Describe the morphology of the red blood cells.
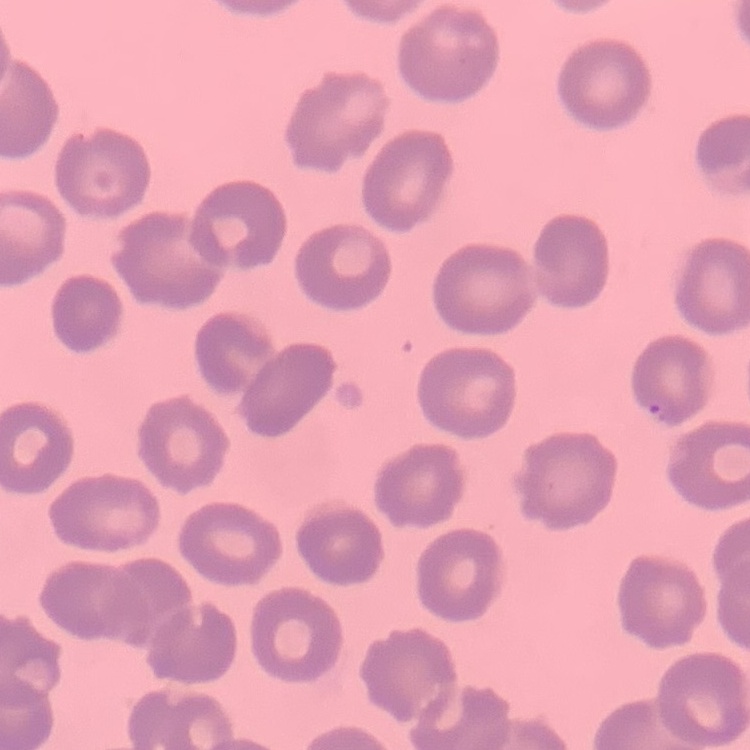
They show no rouleaux formation.

Summary:
  - Stain: Field's or Giemsa
  - Preparation: thin blood smear
  - Image type: square crop of a larger photomicrograph